Assess this cell for malaria.
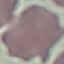

It is uninfected.

Giemsa-stained preparation. Photographed with a smartphone camera at the microscope eyepiece. Automatically extracted cell patch, resized to 64 × 64 pixels. Thin blood film.